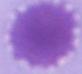
{
  "identification": "erythrocyte",
  "magnification": "1000x",
  "modality": "micrograph"
}